Locate and identify every blood parasite.
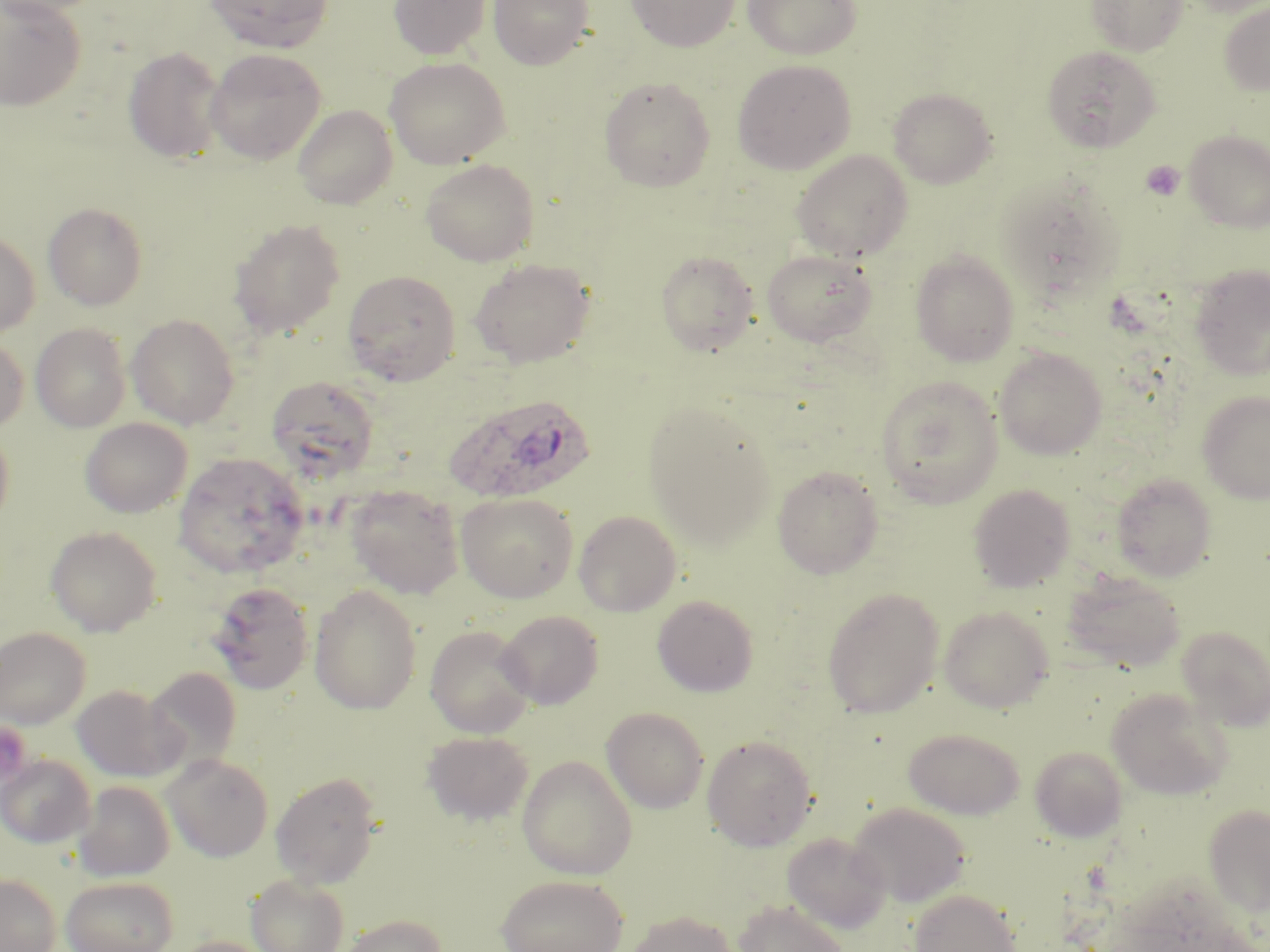

Approximate bounding boxes as named x1/y1/x2/y2 corners in pixels.
Plasmodium ovale-infected red blood cells: (x1=442, y1=393, x2=596, y2=505).
No Plasmodium falciparum, Plasmodium malariae, Plasmodium vivax, Babesia divergens, or Trypanosoma brucei observed.

{
  "slide_level_diagnosis": "Plasmodium ovale",
  "stain": "May-Grünwald-Giemsa",
  "image_size": "1270×952 pixels",
  "uninfected_red_blood_cell_locations": "approximate bounding boxes as named x1/y1/x2/y2 corners in pixels: (x1=0, y1=0, x2=106, y2=17), (x1=1, y1=0, x2=87, y2=111), (x1=203, y1=0, x2=334, y2=53), (x1=389, y1=0, x2=490, y2=60), (x1=489, y1=0, x2=593, y2=69), (x1=626, y1=0, x2=741, y2=51), (x1=742, y1=0, x2=863, y2=59), (x1=1087, y1=0, x2=1188, y2=56), (x1=1184, y1=0, x2=1270, y2=16), (x1=1219, y1=2, x2=1270, y2=95), (x1=1042, y1=45, x2=1161, y2=152), (x1=123, y1=46, x2=227, y2=164), (x1=206, y1=48, x2=325, y2=164), (x1=385, y1=57, x2=509, y2=168), (x1=732, y1=59, x2=856, y2=174), (x1=599, y1=77, x2=716, y2=192), (x1=888, y1=87, x2=997, y2=189), (x1=293, y1=104, x2=397, y2=209), (x1=1184, y1=130, x2=1270, y2=232), (x1=791, y1=149, x2=912, y2=261), (x1=420, y1=158, x2=540, y2=267), (x1=998, y1=176, x2=1125, y2=302), (x1=42, y1=202, x2=148, y2=310), (x1=229, y1=219, x2=345, y2=339), (x1=0, y1=230, x2=40, y2=338), (x1=761, y1=248, x2=877, y2=347), (x1=655, y1=250, x2=758, y2=355), (x1=911, y1=250, x2=1019, y2=366), (x1=469, y1=259, x2=595, y2=368), (x1=1190, y1=264, x2=1270, y2=380), (x1=343, y1=270, x2=460, y2=386), (x1=127, y1=314, x2=239, y2=429), (x1=31, y1=323, x2=131, y2=431), (x1=0, y1=335, x2=28, y2=432), (x1=995, y1=347, x2=1108, y2=460), (x1=267, y1=375, x2=379, y2=481), (x1=876, y1=375, x2=1003, y2=507), (x1=1197, y1=390, x2=1270, y2=504), (x1=642, y1=400, x2=775, y2=546), (x1=81, y1=418, x2=192, y2=518), (x1=0, y1=424, x2=14, y2=531), (x1=174, y1=452, x2=309, y2=578), (x1=772, y1=466, x2=884, y2=579), (x1=1112, y1=473, x2=1216, y2=582), (x1=968, y1=483, x2=1076, y2=592), (x1=346, y1=484, x2=464, y2=599), (x1=457, y1=492, x2=578, y2=603), (x1=573, y1=510, x2=681, y2=617), (x1=46, y1=526, x2=161, y2=637), (x1=1061, y1=570, x2=1186, y2=672), (x1=209, y1=582, x2=315, y2=695), (x1=309, y1=584, x2=422, y2=714), (x1=822, y1=587, x2=944, y2=719), (x1=652, y1=594, x2=759, y2=697), (x1=938, y1=605, x2=1054, y2=712), (x1=497, y1=610, x2=604, y2=709), (x1=425, y1=625, x2=536, y2=738), (x1=0, y1=627, x2=91, y2=728), (x1=1178, y1=627, x2=1270, y2=731), (x1=145, y1=667, x2=242, y2=773), (x1=72, y1=685, x2=185, y2=783), (x1=1106, y1=689, x2=1232, y2=800), (x1=602, y1=707, x2=709, y2=813), (x1=902, y1=727, x2=1024, y2=819), (x1=422, y1=731, x2=534, y2=826), (x1=702, y1=734, x2=818, y2=851), (x1=1030, y1=746, x2=1127, y2=842), (x1=0, y1=755, x2=95, y2=848), (x1=162, y1=755, x2=274, y2=861), (x1=517, y1=755, x2=637, y2=879), (x1=270, y1=772, x2=381, y2=889), (x1=74, y1=781, x2=175, y2=881), (x1=848, y1=802, x2=970, y2=907), (x1=1203, y1=804, x2=1270, y2=916), (x1=782, y1=832, x2=891, y2=933), (x1=0, y1=873, x2=61, y2=952), (x1=246, y1=874, x2=349, y2=952), (x1=496, y1=874, x2=629, y2=952), (x1=60, y1=875, x2=178, y2=952), (x1=909, y1=888, x2=1022, y2=952), (x1=734, y1=899, x2=850, y2=952), (x1=626, y1=910, x2=738, y2=952), (x1=337, y1=915, x2=448, y2=952), (x1=170, y1=935, x2=280, y2=952)",
  "modality": "light microscopy",
  "field_of_view": "one of a larger specimen",
  "preparation": "thin blood smear",
  "magnification": "1000x",
  "platelet_locations": "approximate bounding boxes as named x1/y1/x2/y2 corners in pixels: (x1=1141, y1=160, x2=1184, y2=201), (x1=0, y1=720, x2=32, y2=789)"
}